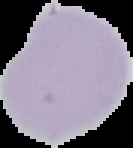

{
  "malaria_status": "uninfected",
  "preparation": "thin blood film",
  "image_type": "segmented cell region on a black background",
  "image_size": "133×148 pixels"
}